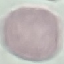

Summary:
  - Malaria status: uninfected
  - Capture: smartphone through the microscope eyepiece
  - Image type: cell patch, automatically extracted from a larger field of view and resized to 64 × 64 pixels
  - Preparation: thin blood film
  - Stain: Giemsa